Locate malaria parasites and leukocytes.
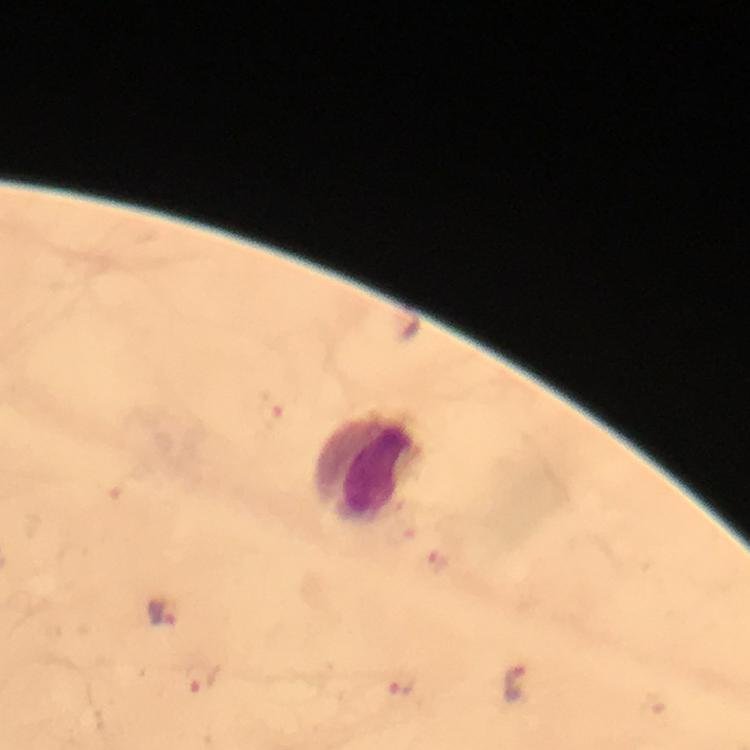

Approximate centers as {x, y} in pixels.
Malaria parasites: {271, 408}, {436, 563}, {167, 613}, {200, 681}, {404, 685}, {520, 686}.
Leukocytes: {368, 470}.

From a malaria diagnostic workup. 100x magnification. Image is 750×750 pixels. Immersion oil applied. Smartphone photograph taken through a microscope. Giemsa-stained preparation. Thick blood smear. A crop from one field of view.